Assess this cell for malaria.
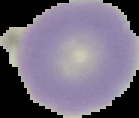

Uninfected.

From a thin blood smear. Image is 139×118 pixels. Segmented cell region on a black background.